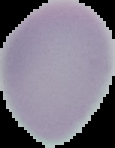
malaria_status: uninfected
image_type: segmented cell region with the area outside set to black
image_size: 115×148 pixels
preparation: thin blood film